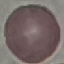

Summary:
  - Malaria status: uninfected
  - Stain: Giemsa
  - Preparation: thin blood film
  - Capture: smartphone camera at the microscope eyepiece
  - Image type: automatically extracted cell patch, resized to 64 × 64 pixels